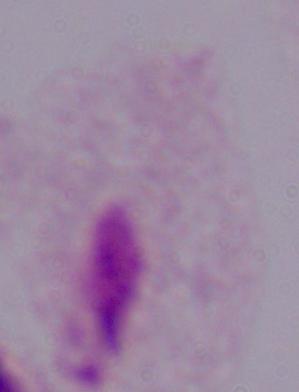

Micrograph. Captured at 1000x magnification. A trichomonad is seen.